Locate every blood parasite and identify its species.
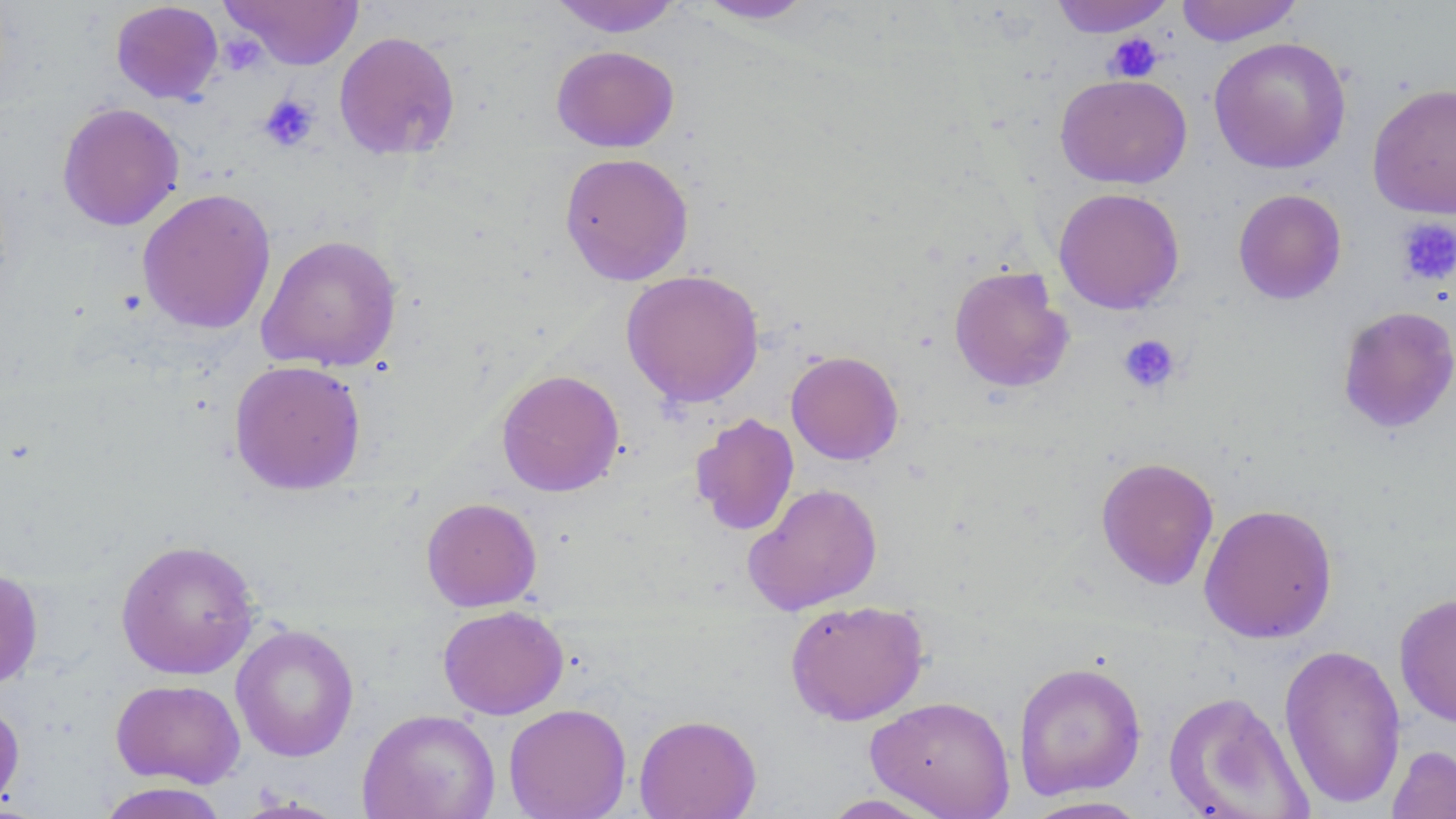

No blood parasites seen.

Approximate bounding boxes as (x1,y1)-(x2,y2) corner pairs in pixels. Uninfected red blood cell locations: (222,0)-(364,70), (549,0)-(684,37), (692,0)-(819,24), (1175,0)-(1303,46), (111,1)-(223,104), (1049,1)-(1175,37), (333,30)-(461,161), (1208,36)-(1351,174), (551,45)-(680,152), (1055,73)-(1192,188), (1368,82)-(1456,218), (57,102)-(184,231), (559,152)-(694,286), (137,187)-(276,335), (1053,187)-(1185,314), (1233,188)-(1347,304), (256,233)-(403,372), (948,265)-(1074,393), (620,268)-(765,408), (1337,305)-(1456,433), (785,350)-(904,465), (228,359)-(367,495), (496,368)-(625,497), (691,413)-(799,536), (1095,456)-(1220,590), (743,482)-(883,616), (421,497)-(542,612), (1198,502)-(1338,644), (115,539)-(260,680), (0,567)-(44,690), (1394,592)-(1456,728), (785,599)-(930,726), (438,605)-(569,720), (231,624)-(359,762), (1278,642)-(1406,809), (1013,660)-(1147,800), (111,678)-(246,788), (1162,690)-(1312,818), (865,695)-(1015,818), (0,698)-(25,812), (503,703)-(632,818), (357,708)-(501,819), (634,714)-(762,818), (1386,743)-(1456,819), (94,782)-(232,819), (816,793)-(951,818), (231,795)-(350,818), (1020,796)-(1156,818). Platelet locations: (224,33)-(267,76), (1103,33)-(1163,82), (258,94)-(320,152), (1394,217)-(1456,287), (1118,334)-(1181,394). Slide-level diagnosis: no evidence of blood parasites. Thin blood smear. May-Grünwald-Giemsa-stained preparation. Image is 1456×819 pixels. One field of a larger specimen. 1000x magnification. Light microscopy.